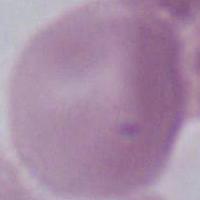

identification: erythrocyte
magnification: 1000x
modality: micrograph